Classify this cell by malaria status.
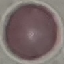
It is uninfected.

Summary:
  - Image type: cell patch, automatically extracted from a larger field of view and resized to 64 × 64 pixels
  - Capture: smartphone through the microscope eyepiece
  - Stain: Giemsa
  - Preparation: thin blood smear